Identify the preparation type.
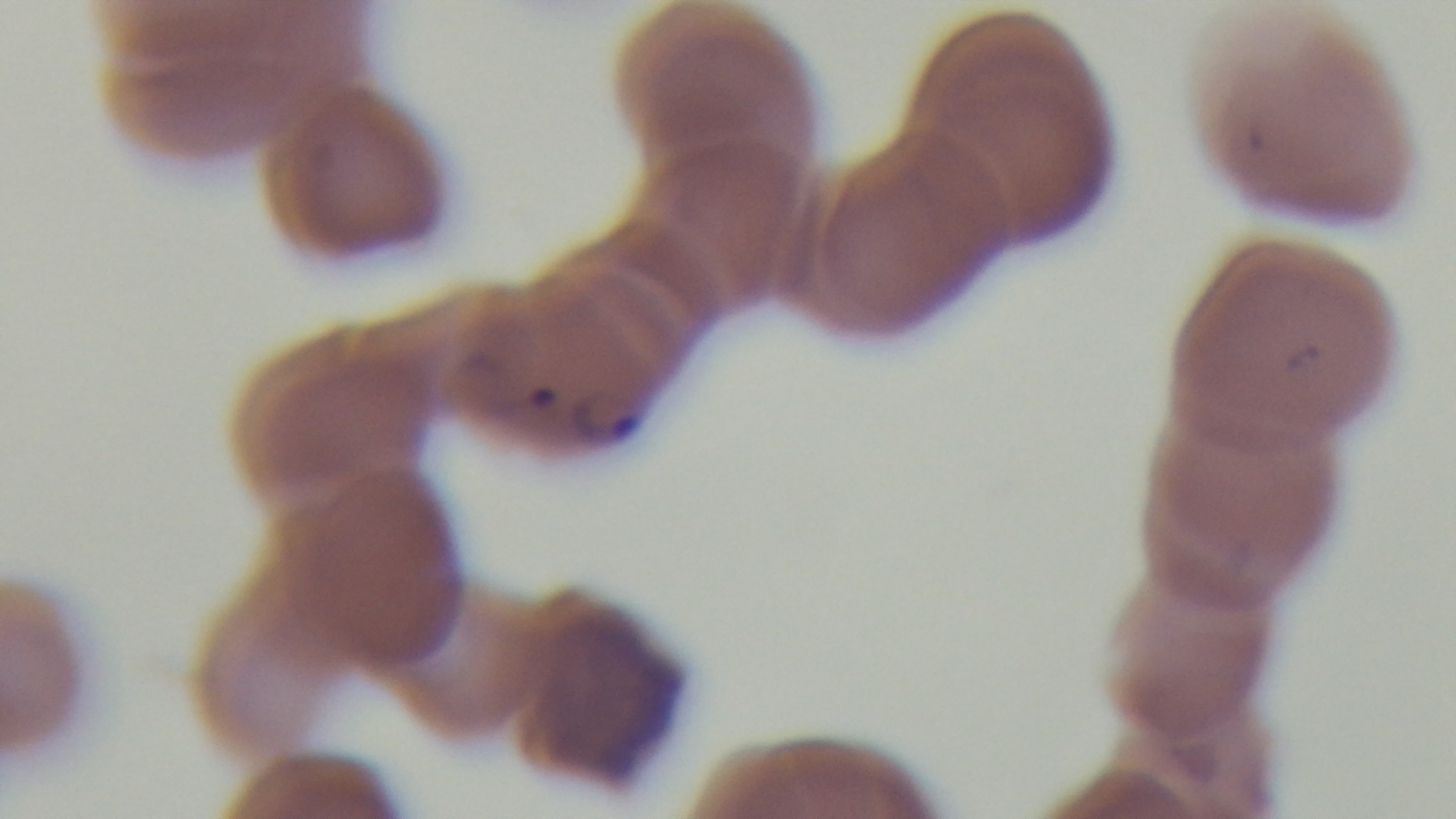

A thin smear.

objective = 100x oil immersion
stain = Giemsa
malaria status = positive
field of view = one from the slide
modality = light microscopy
capture = mounted 4K digital camera